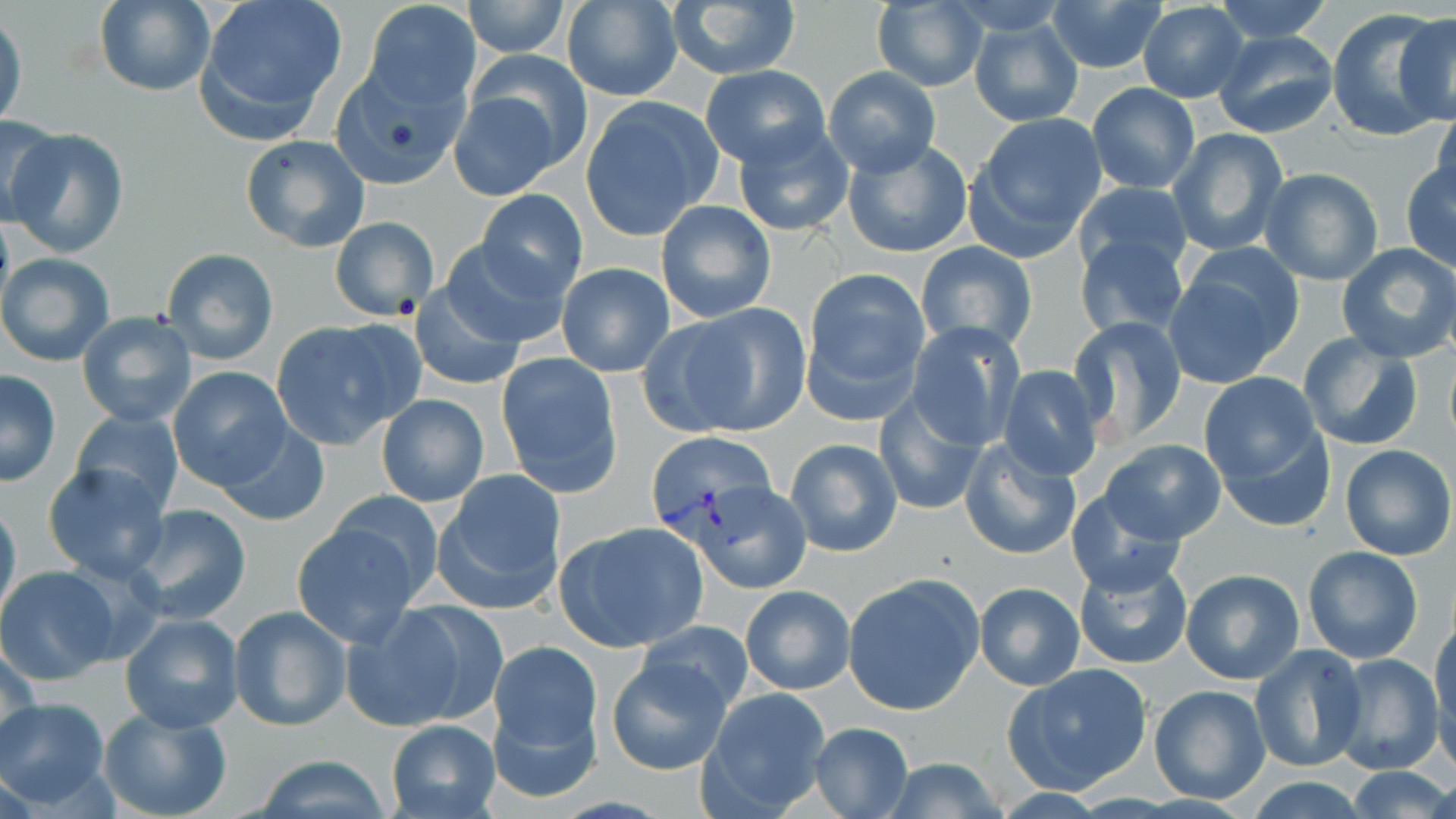
Summary:
  - Coordinate format: approximate bounding boxes as (x1,y1)-(x2,y2) corner pairs in pixels
  - Plasmodium vivax-infected red blood cell locations: (645,431)-(781,554)
  - Uninfected red blood cell locations: (196,0)-(349,141), (1212,0)-(1336,42), (94,1)-(216,97), (362,1)-(481,112), (461,1)-(571,57), (665,1)-(802,81), (1044,1)-(1167,76), (560,2)-(681,104), (869,2)-(987,90), (1136,2)-(1249,103), (1327,9)-(1447,141), (0,11)-(26,131), (1385,12)-(1456,132), (967,16)-(1084,127), (1211,29)-(1339,139), (468,48)-(592,172), (329,63)-(469,190), (702,65)-(829,167), (822,66)-(941,176), (1087,83)-(1200,194), (446,85)-(574,200), (581,97)-(722,238), (1430,105)-(1456,209), (0,112)-(66,224), (966,112)-(1109,257), (731,119)-(856,237), (6,126)-(129,258), (1168,127)-(1290,258), (240,134)-(370,252), (844,139)-(971,257), (1401,161)-(1456,271), (1259,167)-(1384,286), (1071,182)-(1192,282), (476,189)-(587,299), (655,201)-(776,322), (329,216)-(439,321), (1074,233)-(1190,340), (438,237)-(569,349), (1338,241)-(1456,362), (915,242)-(1038,353), (161,247)-(279,366), (1168,247)-(1302,382), (1,252)-(117,367), (557,263)-(673,377), (802,267)-(931,415), (410,284)-(525,391), (652,304)-(812,439), (76,310)-(198,427), (1068,316)-(1189,447), (270,318)-(423,449), (906,322)-(1023,450), (1297,332)-(1423,451), (496,353)-(624,496), (999,365)-(1105,480), (167,367)-(292,491), (0,369)-(62,487), (1198,372)-(1327,491), (874,390)-(991,516), (376,392)-(490,507), (71,409)-(185,514), (1213,413)-(1336,532), (216,421)-(330,527), (784,436)-(903,558), (958,437)-(1082,562), (1098,439)-(1227,546), (1339,445)-(1455,561), (41,462)-(172,584), (434,471)-(566,613), (692,483)-(810,595), (1066,488)-(1190,595), (325,489)-(446,605), (0,495)-(21,625), (125,505)-(254,625), (290,519)-(424,644), (554,520)-(709,652), (1301,546)-(1425,664), (1073,554)-(1194,671), (0,566)-(120,686), (1180,568)-(1306,684), (842,574)-(984,715), (972,580)-(1086,691), (740,584)-(854,695), (341,601)-(491,732), (227,605)-(353,732), (1431,609)-(1456,758), (118,611)-(245,734), (634,620)-(757,719), (487,637)-(602,780), (1,642)-(42,760), (1249,643)-(1369,773), (1332,653)-(1443,776), (605,656)-(733,777), (1003,662)-(1153,795), (1147,683)-(1272,805), (698,686)-(834,816), (0,698)-(111,809), (97,705)-(233,819), (384,718)-(501,818), (806,722)-(914,818), (247,754)-(396,818), (874,756)-(1013,818), (1341,767)-(1456,818)
  - Slide-level diagnosis: Plasmodium vivax
  - Stain: May-Grünwald-Giemsa
  - Preparation: thin blood smear
  - Image size: 1456×819 pixels
  - Field of view: one of a larger specimen
  - Magnification: 1000x
  - Modality: light microscopy